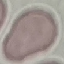

Malaria status: uninfected. Acquired by smartphone through the microscope eyepiece. Giemsa-stained preparation. Thin smear of blood. Cell patch, automatically extracted from a larger field of view and resized to 64 × 64 pixels.